State which parasite is depicted.
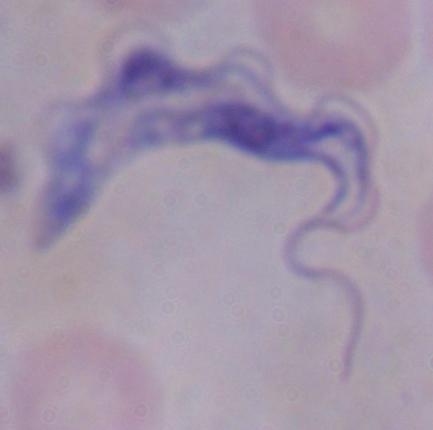
A trypanosome.

magnification: 1000x
modality: micrograph